Locate every blood parasite and identify its species.
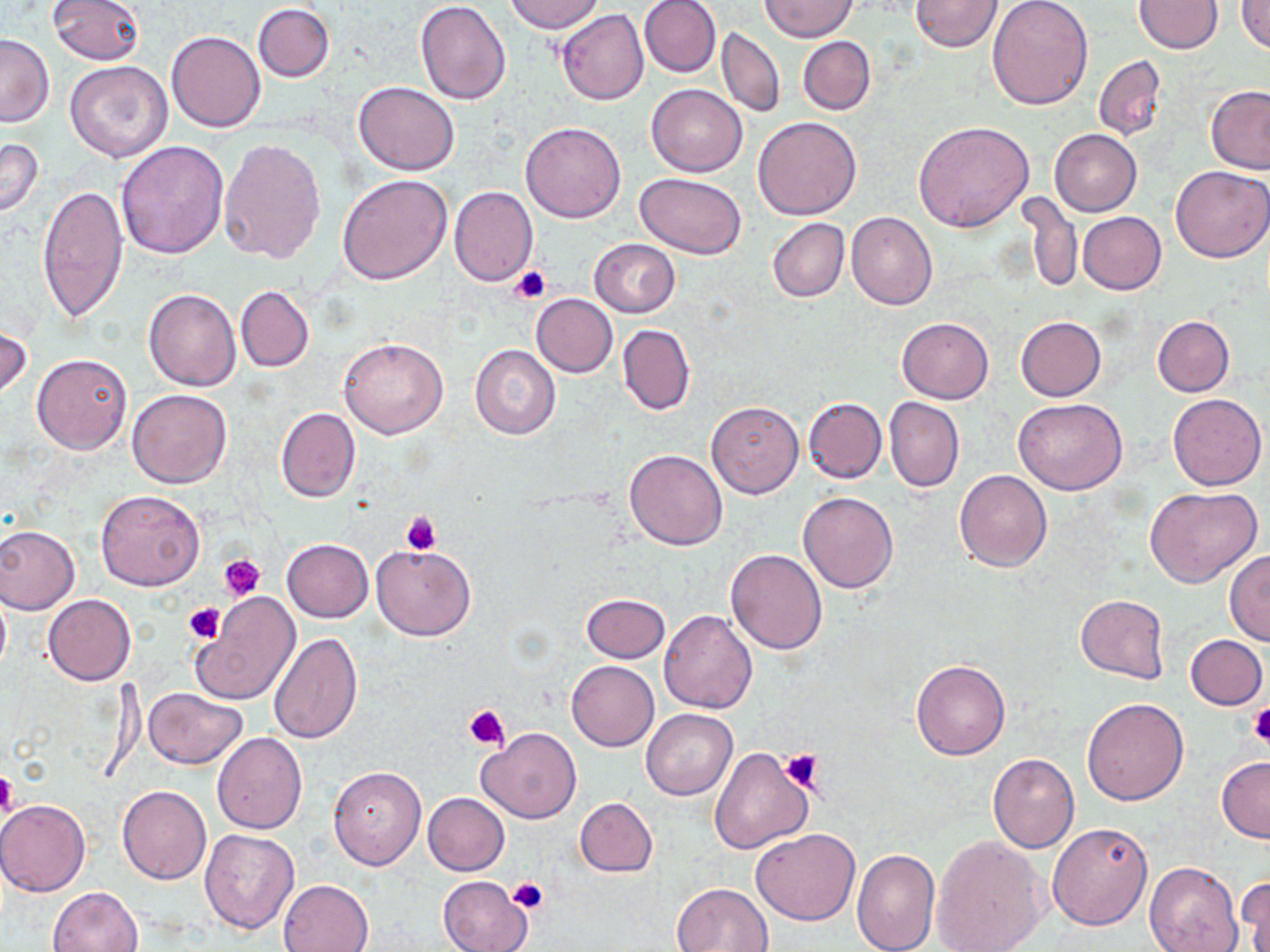

No blood parasites observed.

{
  "slide_level_diagnosis": "no evidence of blood parasites",
  "modality": "optical microscopy",
  "platelet_locations": "approximate bounding boxes as (x1, y1, x2, y2) in pixels: (510, 265, 550, 303), (400, 510, 442, 555), (219, 554, 266, 600), (183, 602, 225, 643), (464, 703, 510, 750), (1248, 706, 1270, 747), (778, 747, 826, 793), (0, 768, 18, 819), (507, 879, 549, 914)",
  "uninfected_red_blood_cell_locations": "approximate bounding boxes as (x1, y1, x2, y2) in pixels: (49, 0, 145, 64), (505, 0, 604, 32), (639, 0, 720, 78), (761, 0, 858, 41), (910, 0, 1004, 52), (987, 0, 1094, 109), (415, 1, 512, 104), (1133, 1, 1224, 53), (1237, 1, 1270, 54), (252, 4, 334, 82), (557, 10, 649, 105), (718, 27, 785, 117), (166, 30, 266, 133), (0, 34, 55, 128), (798, 36, 876, 115), (1094, 56, 1167, 140), (65, 60, 174, 163), (353, 82, 460, 176), (646, 83, 748, 176), (1207, 86, 1270, 175), (754, 116, 861, 219), (521, 121, 626, 222), (912, 122, 1036, 232), (1050, 129, 1142, 216), (0, 137, 44, 220), (219, 138, 327, 263), (115, 140, 229, 259), (1171, 166, 1269, 263), (634, 172, 747, 259), (337, 173, 453, 285), (37, 183, 129, 322), (449, 186, 538, 286), (1020, 190, 1081, 294), (847, 211, 938, 310), (1077, 212, 1166, 294), (767, 217, 849, 303), (589, 238, 681, 317), (235, 286, 314, 372), (144, 288, 242, 391), (531, 294, 617, 377), (1152, 316, 1234, 397), (897, 317, 994, 404), (1016, 317, 1106, 401), (0, 323, 31, 402), (617, 324, 695, 416), (339, 336, 447, 439), (470, 344, 560, 439), (32, 354, 132, 455), (127, 389, 232, 488), (1167, 392, 1267, 490), (804, 397, 888, 484), (885, 398, 964, 493), (1014, 398, 1127, 496), (707, 402, 804, 497), (275, 407, 361, 502), (624, 449, 727, 550), (954, 470, 1052, 572), (1144, 487, 1262, 588), (96, 489, 206, 591), (799, 492, 898, 595), (0, 524, 80, 615), (282, 538, 373, 622), (371, 543, 476, 639), (1224, 549, 1270, 646), (725, 550, 827, 654), (0, 589, 10, 679), (190, 592, 300, 705), (42, 593, 137, 686), (581, 593, 671, 663), (1075, 594, 1169, 684), (658, 610, 758, 714), (268, 631, 361, 744), (1185, 633, 1267, 710), (566, 660, 659, 750), (911, 660, 1010, 759), (143, 687, 247, 769), (1082, 698, 1189, 804), (641, 709, 737, 800), (477, 727, 582, 823), (212, 732, 308, 834), (709, 746, 813, 855), (987, 753, 1080, 853), (1217, 756, 1270, 842), (328, 766, 425, 871), (116, 785, 210, 884), (422, 792, 510, 876), (575, 797, 657, 877), (1, 799, 90, 897), (1048, 822, 1154, 930), (751, 828, 859, 926), (199, 829, 299, 934), (931, 836, 1050, 952), (852, 847, 939, 951), (1145, 861, 1243, 952), (1236, 873, 1270, 952), (437, 876, 531, 952), (278, 879, 375, 952), (673, 882, 774, 951), (48, 886, 143, 951)",
  "stain": "May-Grünwald-Giemsa",
  "field_of_view": "single",
  "image_size": "1270×952 pixels",
  "preparation": "thin blood smear",
  "magnification": "1000x"
}